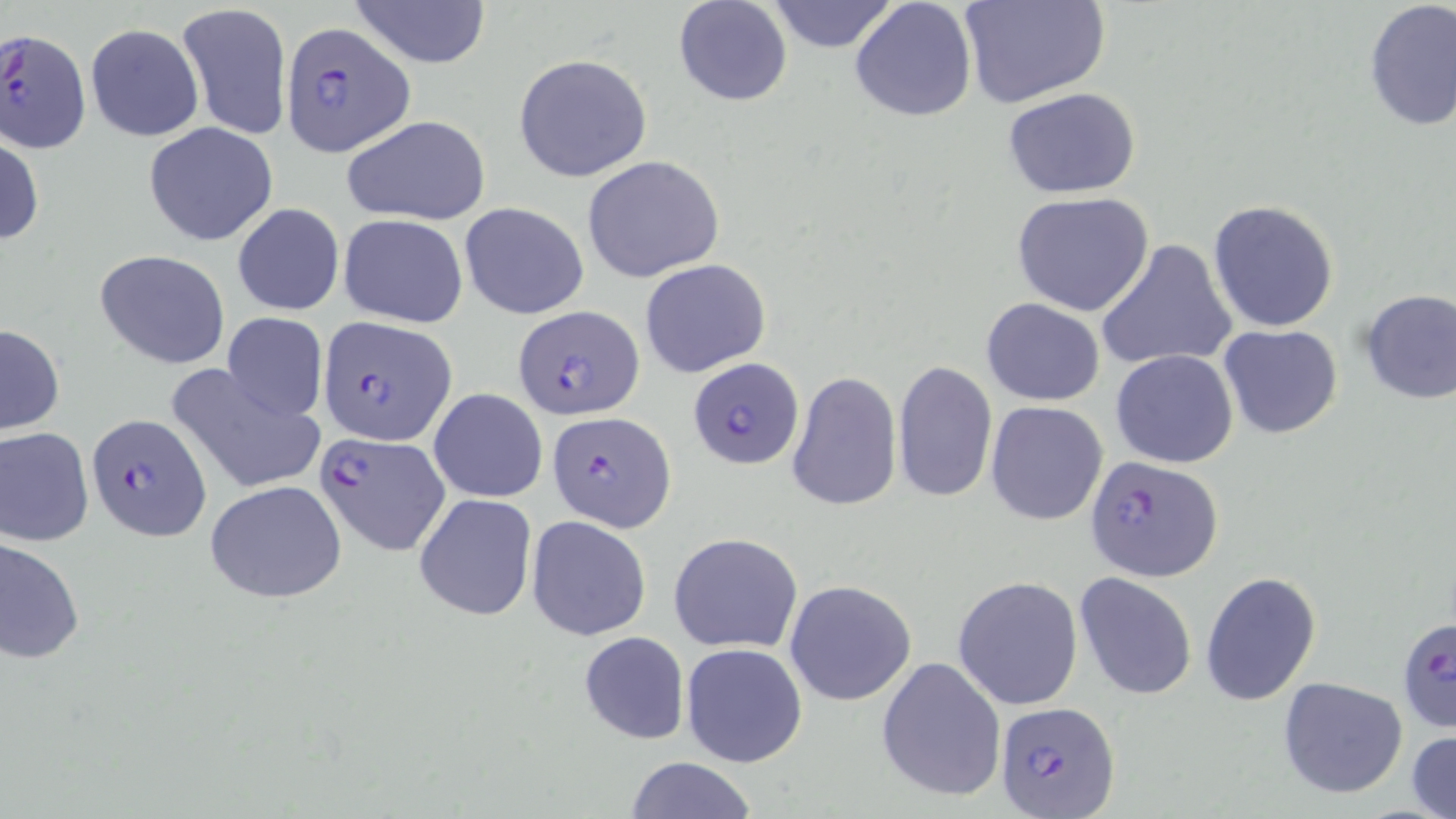
plasmodium_falciparum_infected_red_blood_cell_locations: 'approximate bounding boxes as (x1,y1)-(x2,y2) corner pairs in pixels: (281,23)-(415,156), (0,31)-(92,152), (511,305)-(643,419), (317,316)-(455,445), (686,359)-(804,471), (548,410)-(676,530), (86,412)-(209,540), (315,430)-(451,556), (1086,455)-(1224,581), (1401,609)-(1456,729), (995,700)-(1121,819)'
slide_level_diagnosis: Plasmodium falciparum
uninfected_red_blood_cell_locations: 'approximate bounding boxes as (x1,y1)-(x2,y2) corner pairs in pixels: (349,0)-(492,69), (672,0)-(793,106), (849,0)-(978,124), (964,0)-(1109,110), (764,1)-(898,53), (178,2)-(290,144), (1363,2)-(1456,135), (85,25)-(203,141), (513,53)-(653,182), (1004,89)-(1142,199), (341,114)-(491,227), (143,121)-(278,246), (0,128)-(44,249), (582,155)-(727,283), (1010,192)-(1156,317), (1209,201)-(1339,331), (232,202)-(344,316), (458,202)-(588,320), (339,214)-(468,328), (1097,239)-(1238,372), (96,248)-(231,368), (639,259)-(770,378), (1357,287)-(1456,406), (980,299)-(1106,404), (221,311)-(328,422), (0,323)-(65,436), (1218,323)-(1344,440), (1111,349)-(1239,468), (892,359)-(997,504), (169,364)-(326,496), (786,369)-(902,512), (428,387)-(547,502), (987,401)-(1109,524), (0,426)-(93,545), (205,480)-(349,602), (414,492)-(537,622), (526,516)-(652,641), (668,532)-(803,653), (1,535)-(84,666), (1074,571)-(1198,701), (1201,572)-(1322,705), (953,576)-(1083,711), (784,579)-(916,706), (578,631)-(690,745), (681,642)-(807,767), (876,655)-(1006,803), (1277,676)-(1408,799), (1407,730)-(1456,819), (622,756)-(760,819)'
image_size: 1456×819 pixels
preparation: thin blood smear
field_of_view: single
stain: May-Grünwald-Giemsa
modality: optical microscopy
magnification: 1000x